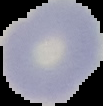

image size = 103×106 pixels
malaria status = uninfected
preparation = thin blood smear
image type = segmented cell region on a black background